Assess this cell for malaria.
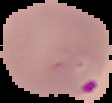
It is parasitized.

Image is 112×103 pixels. From a thin blood smear. Cell region segmented out of the field of view; the surrounding area is masked to black.